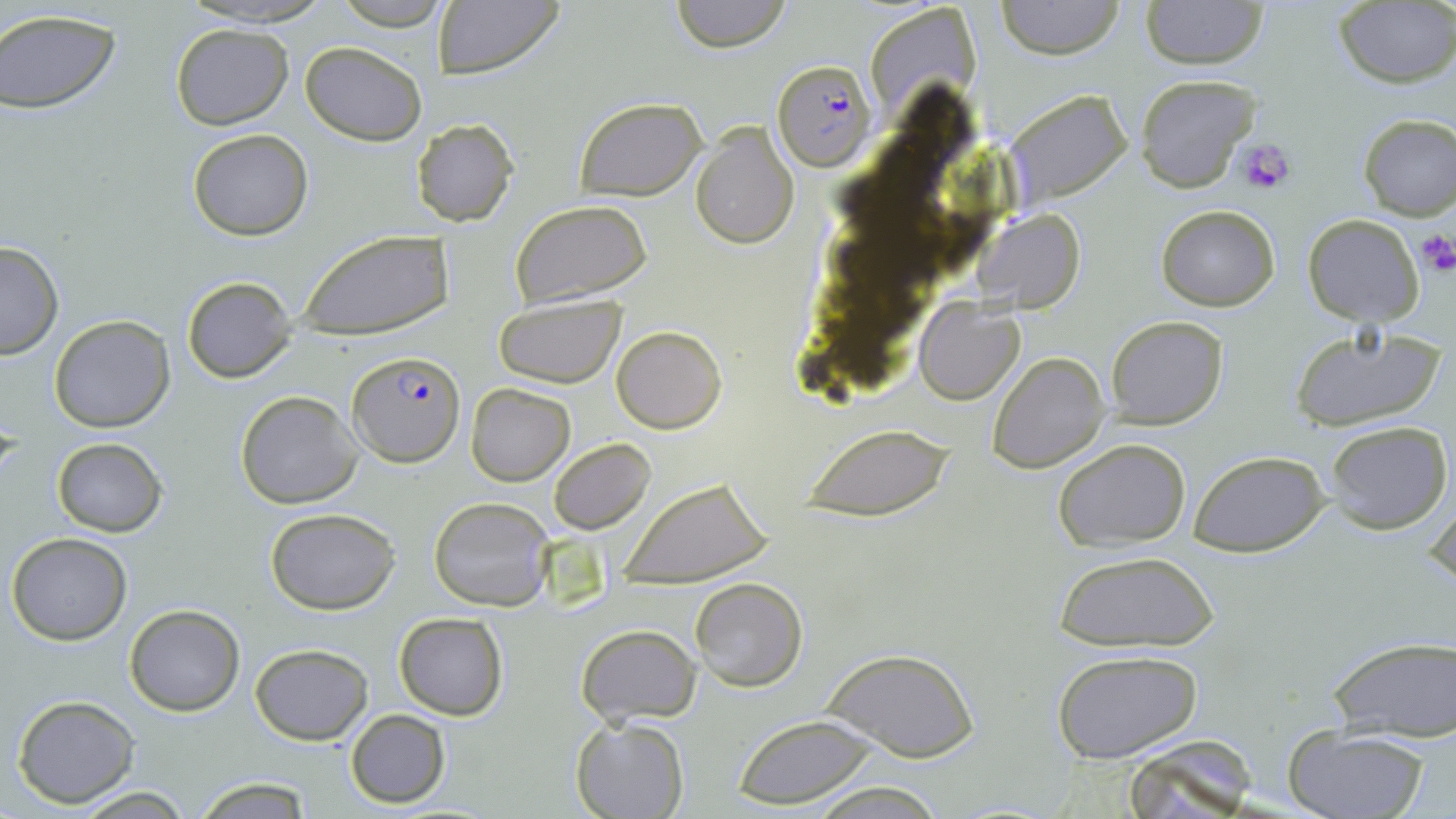
slide_level_diagnosis: Plasmodium falciparum
preparation: thin blood film
platelet_locations: 'approximate bounding boxes as (x1, y1, x2, y2) in pixels: (1236, 137, 1298, 196), (1414, 232, 1456, 277)'
modality: optical microscopy
uninfected_red_blood_cell_locations: 'approximate bounding boxes as (x1, y1, x2, y2) in pixels: (173, 0, 339, 27), (669, 0, 793, 52), (998, 0, 1124, 59), (1139, 0, 1270, 69), (432, 1, 565, 80), (1334, 2, 1455, 88), (871, 3, 980, 111), (0, 10, 123, 116), (170, 23, 292, 129), (300, 41, 428, 146), (1135, 73, 1259, 192), (1003, 90, 1133, 207), (573, 97, 707, 200), (1357, 114, 1456, 220), (409, 118, 521, 227), (691, 123, 799, 250), (187, 129, 313, 241), (509, 200, 655, 313), (1157, 205, 1280, 310), (979, 210, 1084, 311), (1303, 213, 1424, 326), (296, 232, 452, 341), (0, 240, 63, 359), (181, 276, 299, 385), (494, 296, 627, 387), (915, 302, 1023, 403), (48, 314, 175, 433), (1106, 315, 1228, 429), (612, 324, 726, 434), (1288, 325, 1446, 433), (989, 352, 1108, 474), (465, 382, 575, 485), (234, 390, 364, 510), (1324, 420, 1453, 533), (800, 424, 954, 519), (52, 437, 167, 537), (1053, 437, 1192, 551), (549, 438, 655, 533), (1189, 451, 1329, 555), (617, 476, 775, 589), (1426, 488, 1455, 596), (428, 497, 554, 611), (264, 506, 403, 614), (6, 532, 132, 645), (1048, 548, 1224, 653), (689, 576, 809, 693), (125, 605, 245, 715), (394, 612, 508, 719), (576, 624, 701, 725), (1327, 633, 1456, 742), (250, 644, 374, 745), (823, 646, 978, 763), (1051, 647, 1207, 766), (11, 695, 139, 807), (346, 710, 449, 808), (730, 713, 884, 807), (571, 718, 690, 819), (1282, 725, 1433, 819), (1116, 741, 1264, 818), (193, 776, 315, 817), (802, 781, 952, 818), (70, 786, 196, 818)'
image_size: 1456×819 pixels
field_of_view: single
plasmodium_falciparum_infected_red_blood_cell_locations: 'approximate bounding boxes as (x1, y1, x2, y2) in pixels: (771, 58, 878, 172), (349, 349, 464, 466)'
magnification: 1000x
stain: May-Grünwald-Giemsa